Look for Plasmodium parasites.
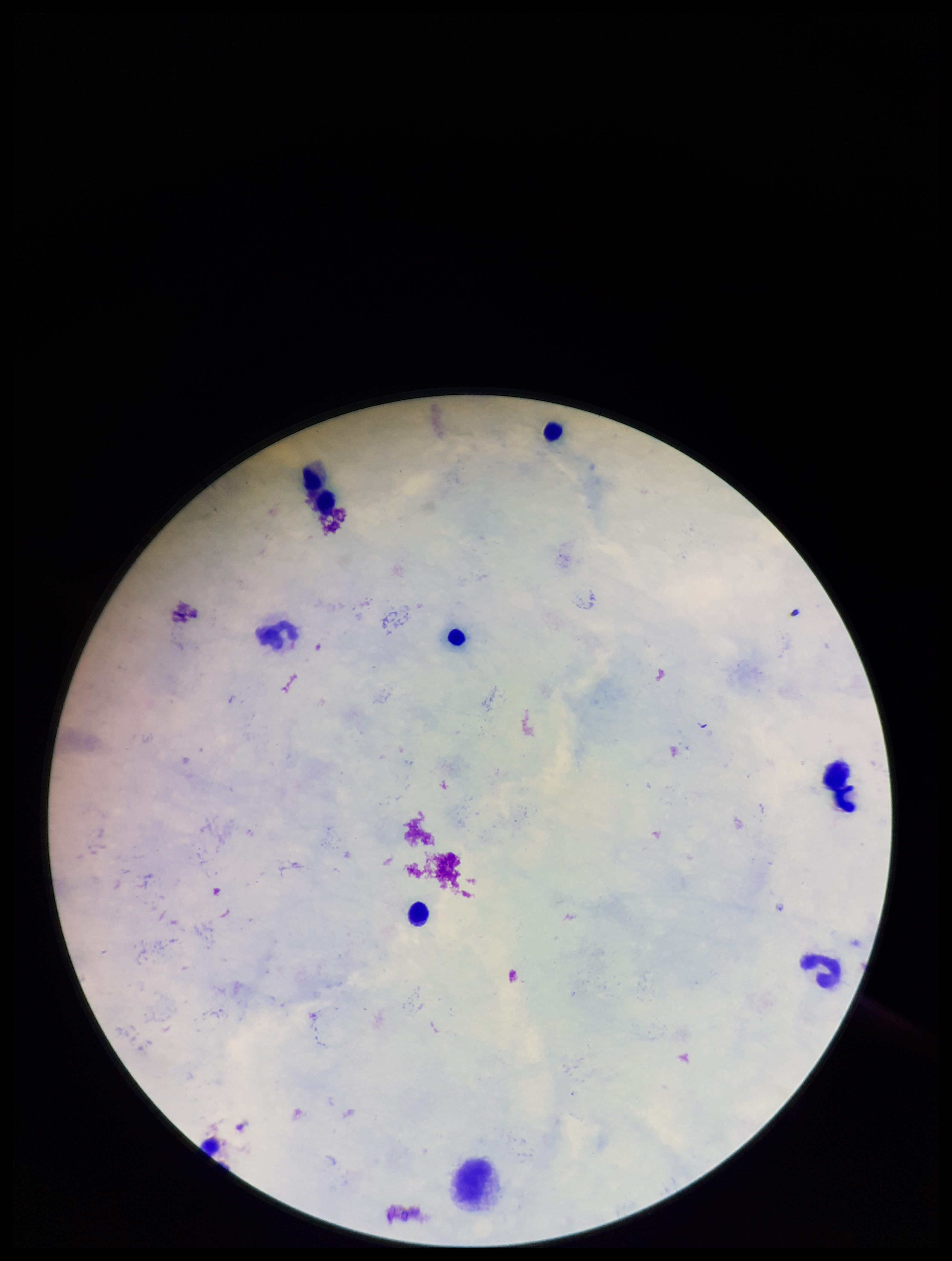

None identified.

Patient malaria status: negative. Preparation: thick blood smear. Parasite count: 0. Giemsa stain. Image is 952×1261 pixels. Leukocyte count: 8. Smartphone photograph taken through the eyepiece of a microscope. Single field of view.